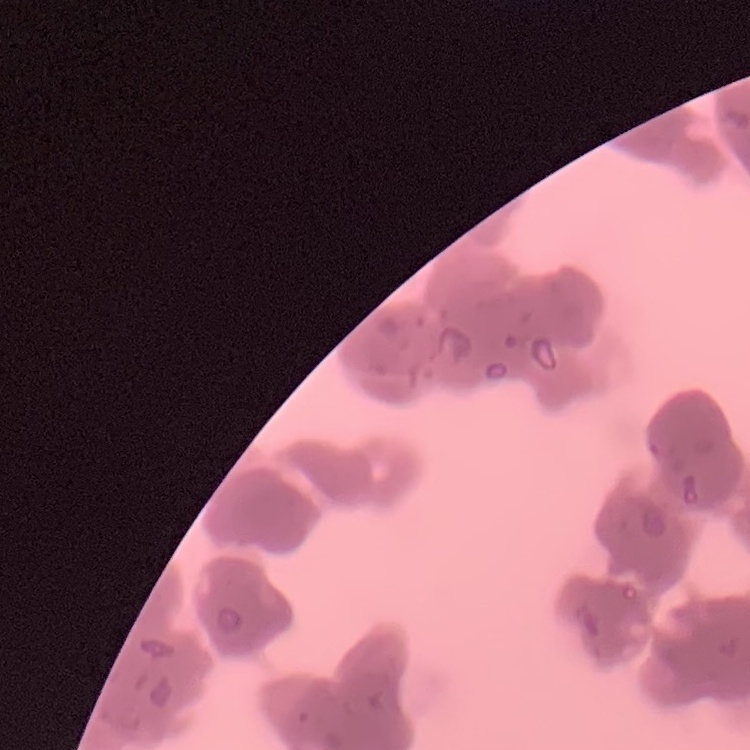

The erythrocytes show rouleaux formation. Field's or Giemsa stain. One tile cut from a larger photomicrograph. Thin peripheral smear.